Report the malaria status of this cell.
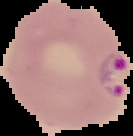

It is parasitized.

{
  "image_size": "133×136 pixels",
  "image_type": "segmented cell region with the area outside set to black",
  "preparation": "thin blood film"
}